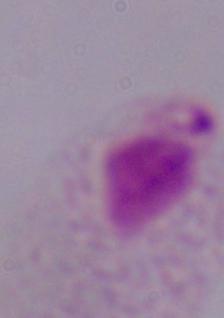

A trichomonad is seen. Photomicrograph. 1000x magnification.